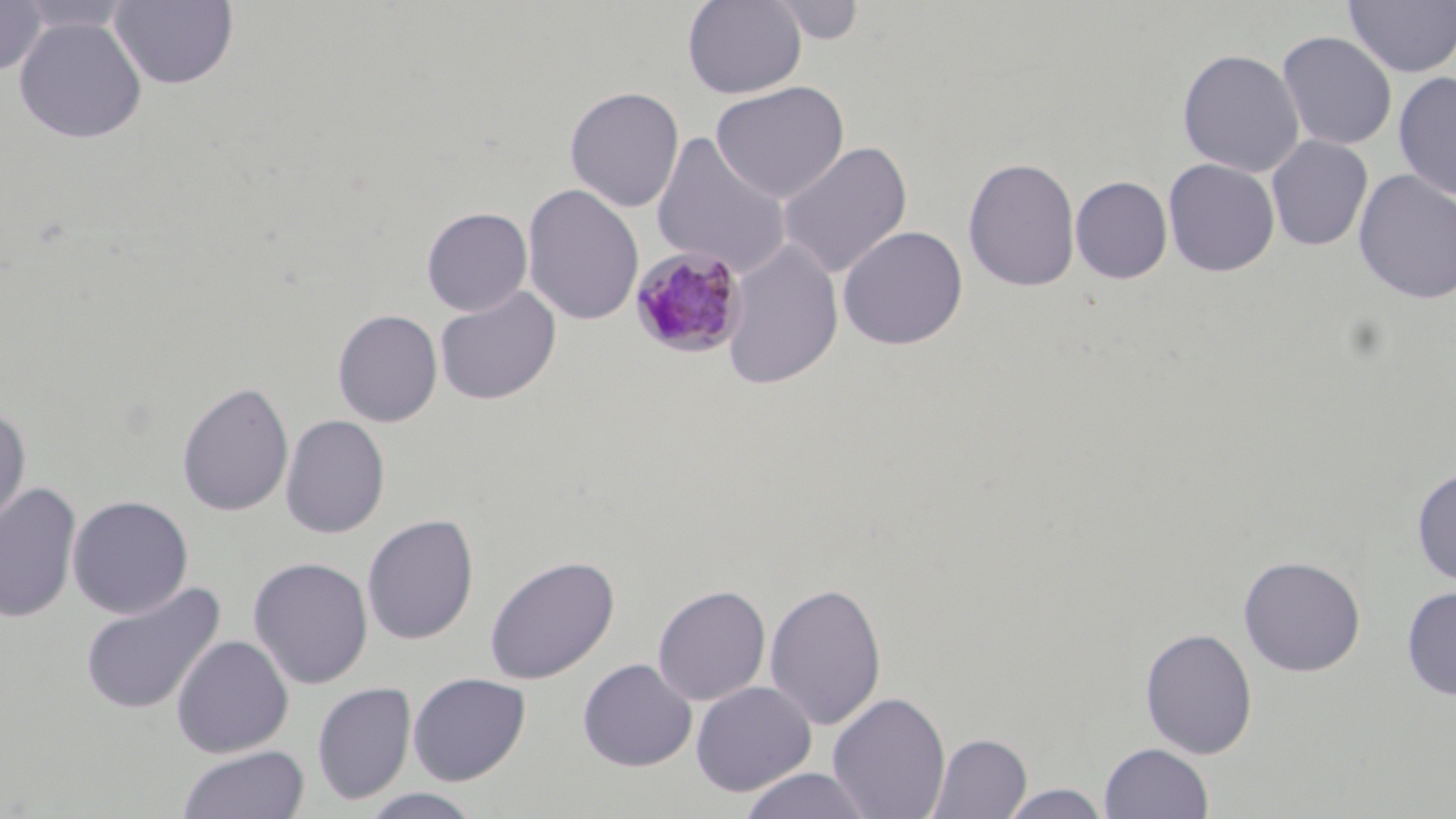
slide_level_diagnosis: Plasmodium malariae
field_of_view: one of a larger specimen
stain: May-Grünwald-Giemsa
image_size: 1456×819 pixels
uninfected_red_blood_cell_locations: 'approximate bounding boxes as named x1/y1/x2/y2 corners in pixels: (x1=15, y1=0, x2=135, y2=35), (x1=109, y1=0, x2=239, y2=90), (x1=683, y1=0, x2=807, y2=99), (x1=1344, y1=0, x2=1456, y2=78), (x1=0, y1=1, x2=48, y2=76), (x1=764, y1=1, x2=868, y2=44), (x1=13, y1=16, x2=147, y2=144), (x1=1276, y1=30, x2=1398, y2=151), (x1=1177, y1=48, x2=1305, y2=178), (x1=1393, y1=71, x2=1456, y2=200), (x1=710, y1=80, x2=849, y2=203), (x1=565, y1=86, x2=685, y2=212), (x1=650, y1=132, x2=792, y2=279), (x1=1266, y1=135, x2=1373, y2=251), (x1=777, y1=140, x2=913, y2=279), (x1=963, y1=156, x2=1081, y2=293), (x1=1163, y1=158, x2=1280, y2=277), (x1=1353, y1=168, x2=1456, y2=306), (x1=1070, y1=175, x2=1172, y2=284), (x1=522, y1=183, x2=644, y2=326), (x1=422, y1=207, x2=533, y2=316), (x1=837, y1=225, x2=968, y2=350), (x1=720, y1=238, x2=844, y2=390), (x1=434, y1=286, x2=561, y2=406), (x1=332, y1=309, x2=443, y2=427), (x1=176, y1=380, x2=294, y2=518), (x1=0, y1=406, x2=32, y2=534), (x1=280, y1=414, x2=390, y2=539), (x1=1412, y1=467, x2=1456, y2=586), (x1=0, y1=483, x2=81, y2=623), (x1=67, y1=495, x2=193, y2=619), (x1=361, y1=514, x2=480, y2=645), (x1=1238, y1=554, x2=1366, y2=676), (x1=484, y1=555, x2=620, y2=685), (x1=248, y1=557, x2=373, y2=690), (x1=79, y1=580, x2=226, y2=716), (x1=764, y1=582, x2=887, y2=731), (x1=652, y1=584, x2=771, y2=706), (x1=1401, y1=586, x2=1456, y2=701), (x1=1139, y1=627, x2=1258, y2=759), (x1=171, y1=634, x2=294, y2=758), (x1=577, y1=658, x2=697, y2=772), (x1=408, y1=672, x2=531, y2=785), (x1=690, y1=680, x2=816, y2=797), (x1=312, y1=681, x2=416, y2=805), (x1=827, y1=691, x2=951, y2=819), (x1=926, y1=732, x2=1032, y2=819), (x1=1099, y1=742, x2=1214, y2=818), (x1=178, y1=745, x2=309, y2=819), (x1=737, y1=767, x2=877, y2=819), (x1=998, y1=783, x2=1112, y2=819), (x1=358, y1=788, x2=485, y2=819)'
magnification: 1000x
modality: optical microscopy
preparation: thin blood film
plasmodium_malariae_infected_red_blood_cell_locations: 'approximate bounding boxes as named x1/y1/x2/y2 corners in pixels: (x1=628, y1=246, x2=748, y2=359)'